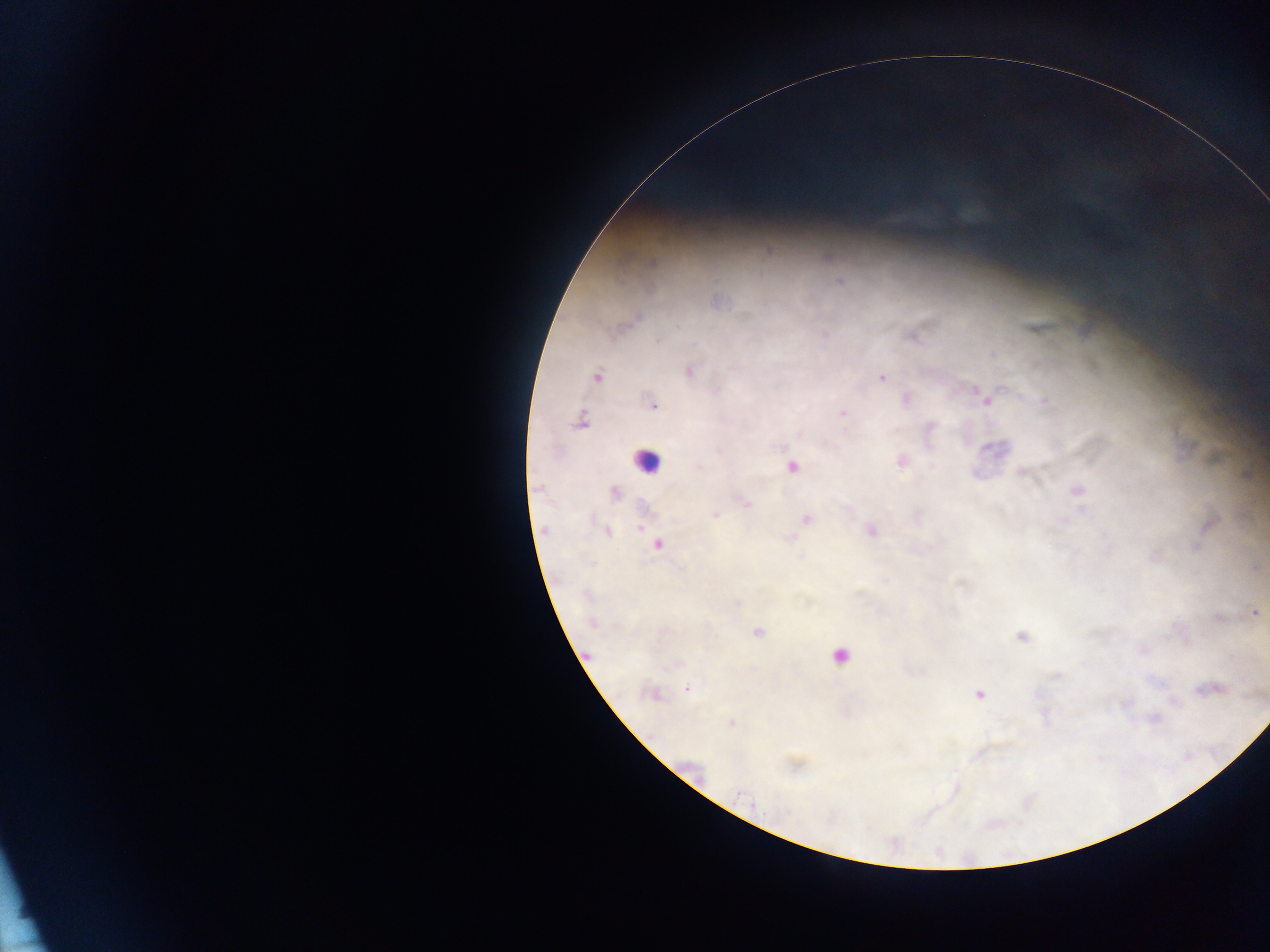

Approximate centers as (x, y) in pixels.
Summary:
  - Plasmodium parasite locations: (881, 376), (596, 377), (653, 405), (842, 414), (807, 518), (1254, 612), (687, 687), (893, 844)
  - Leukocyte locations: (637, 462)
  - Country: Ghana
  - Capture: mobile-phone photograph through a microscope
  - Field of view: single
  - Image size: 1270×952 pixels
  - Preparation: thick blood smear